Look for Plasmodium parasites.
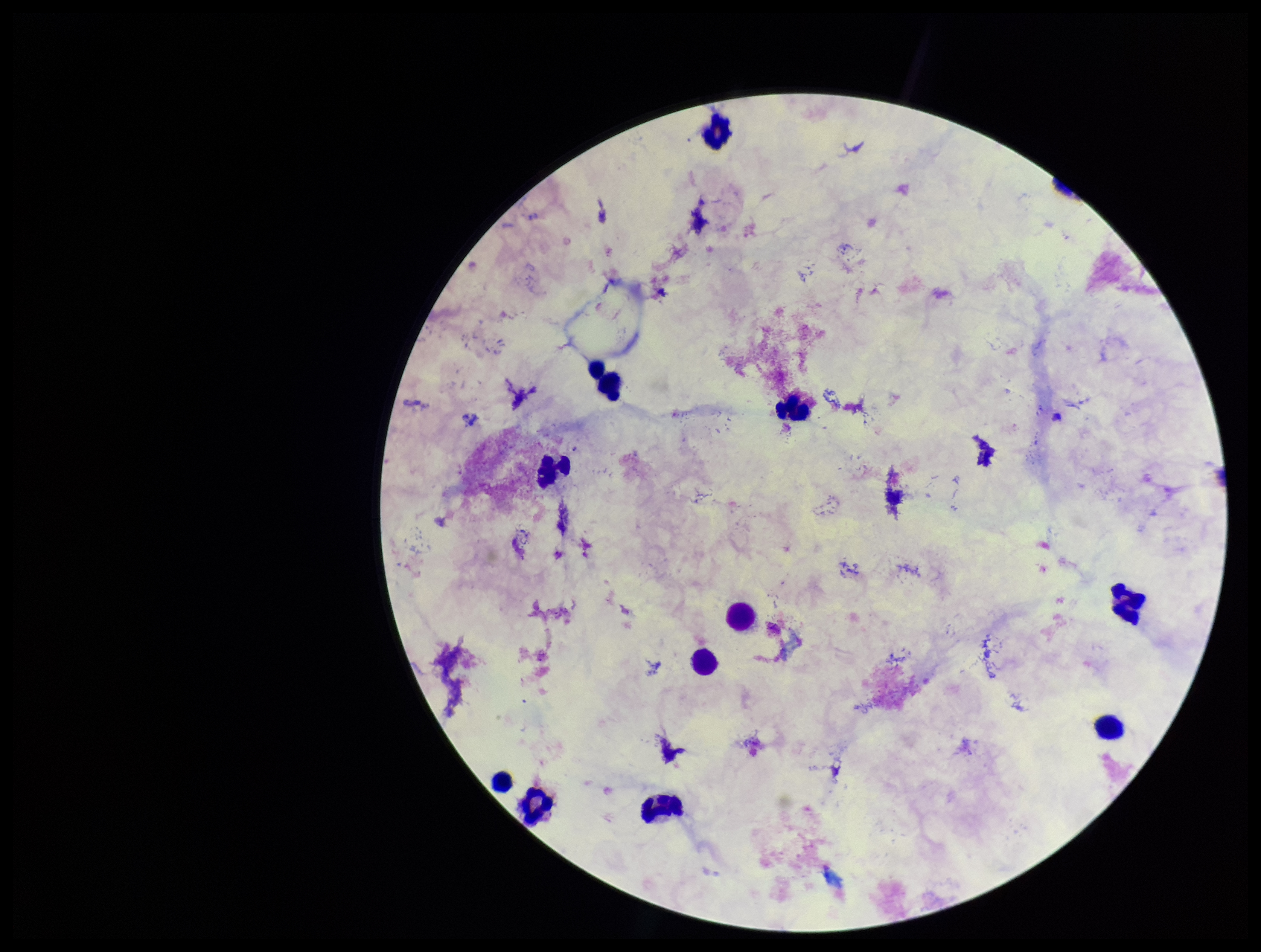

None seen.

preparation = thick blood smear
patient malaria status = negative
stain = Giemsa
image size = 1261×952 pixels
parasite count = 0
field of view = single
leukocyte count = 15
capture = smartphone photograph through the microscope eyepiece